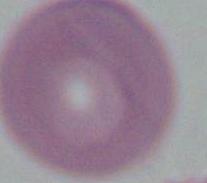
1000x magnification. Photomicrograph. A red blood cell is shown.